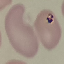

{
  "result": "no malaria parasites seen",
  "preparation": "thin blood film",
  "image_type": "cell patch, automatically extracted from a larger field of view and resized to 64 × 64 pixels",
  "capture": "smartphone through the microscope eyepiece",
  "stain": "Giemsa"
}